Look for Plasmodium parasites.
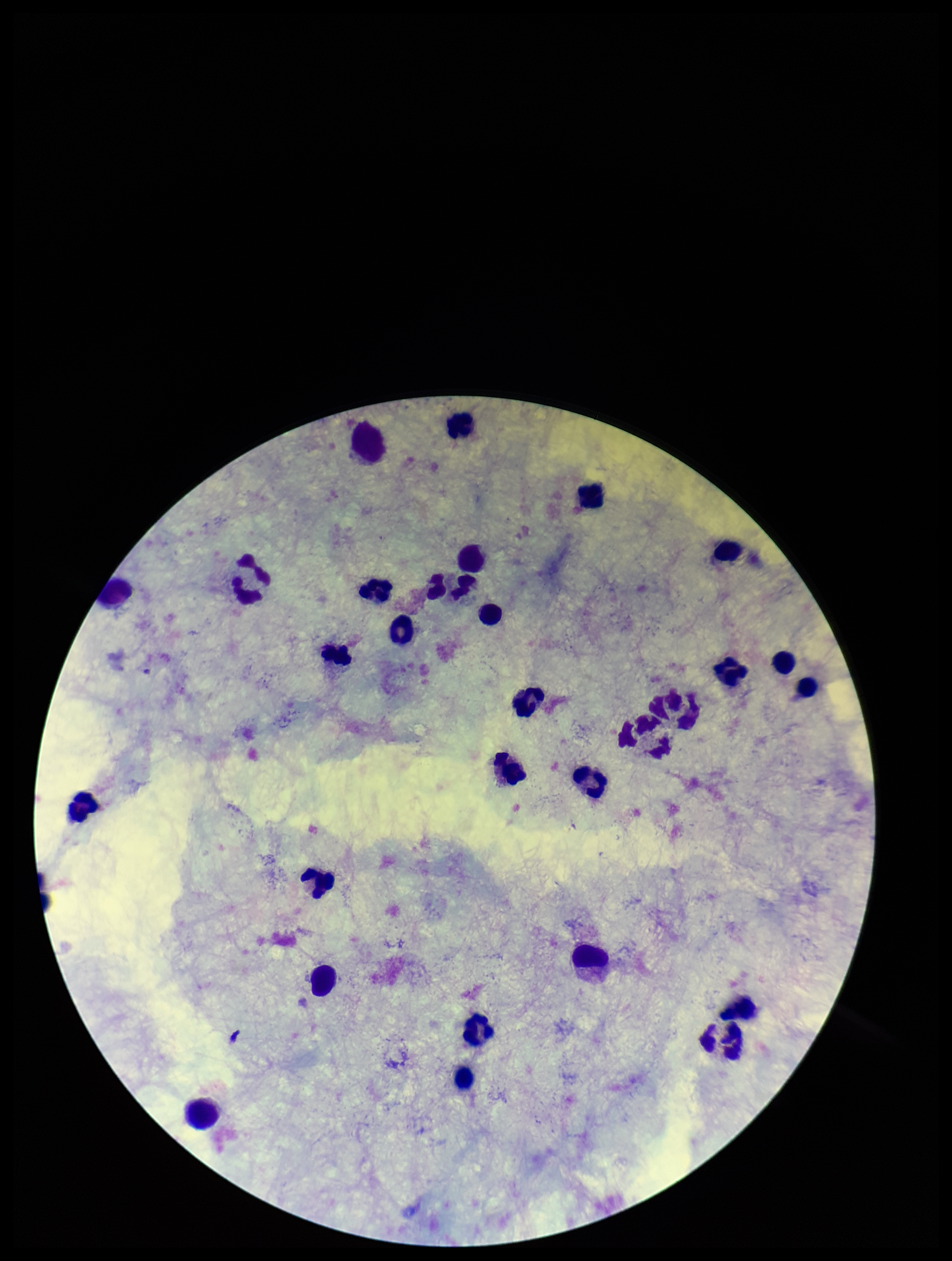
None identified.

Summary:
  - Field of view: one from this slide
  - Stain: Giemsa
  - Leukocyte count: 29
  - Capture: smartphone photograph through the microscope eyepiece
  - Image size: 952×1261 pixels
  - Parasite count: 0
  - Patient malaria status: negative
  - Preparation: thick